State which parasite is depicted.
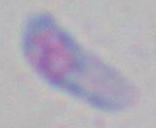
This is Toxoplasma gondii.

{
  "modality": "micrograph",
  "magnification": "1000x"
}